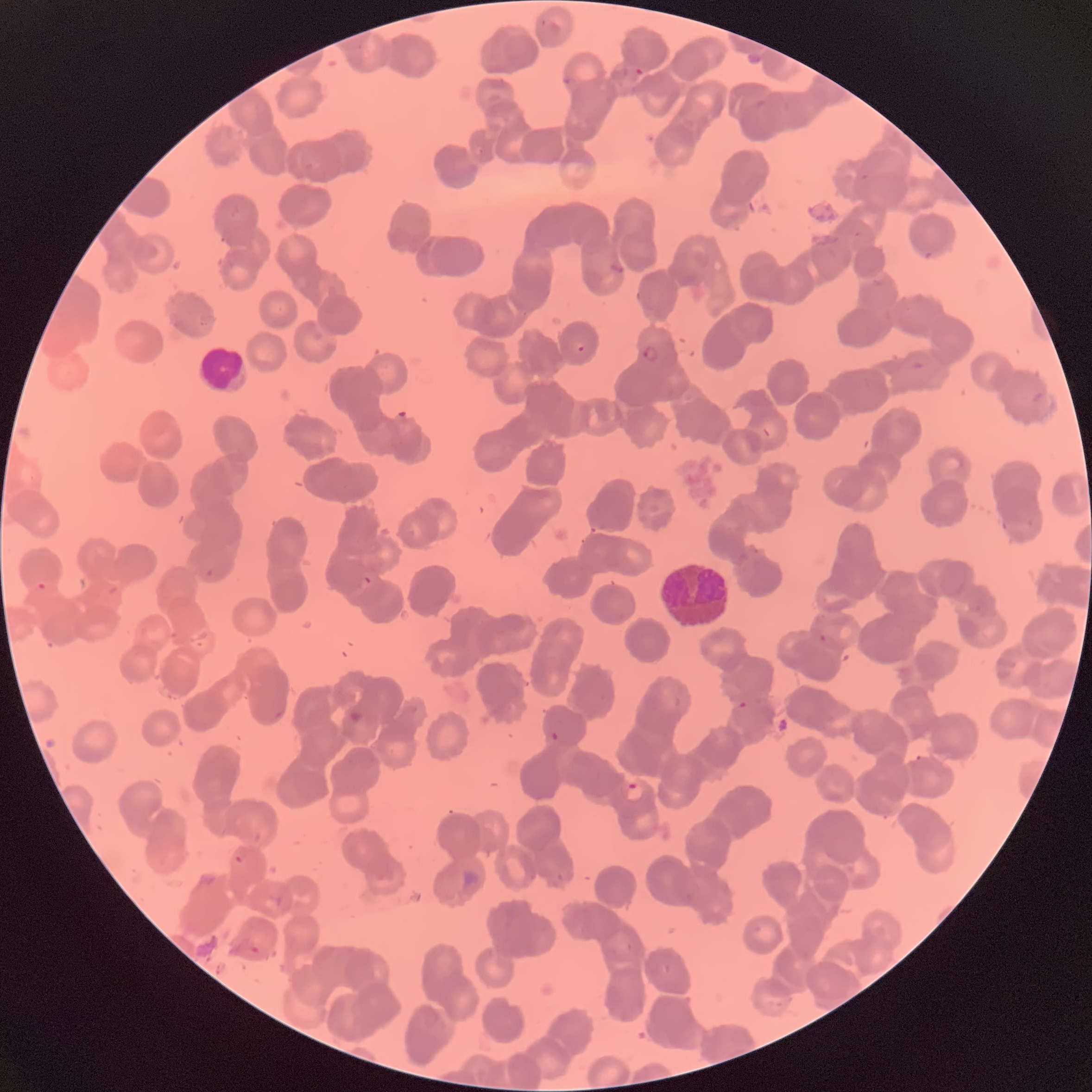

Summary:
  - Coordinate format: approximate bounding boxes as named x1/y1/x2/y2 corners in pixels
  - White blood cell locations: (x1=199, y1=344, x2=248, y2=395)
  - Plasmodium parasite locations: (x1=634, y1=67, x2=645, y2=77), (x1=560, y1=74, x2=573, y2=87), (x1=610, y1=256, x2=624, y2=274), (x1=577, y1=342, x2=586, y2=353), (x1=643, y1=344, x2=660, y2=364), (x1=205, y1=568, x2=215, y2=577), (x1=362, y1=576, x2=373, y2=585), (x1=36, y1=581, x2=47, y2=591), (x1=817, y1=634, x2=842, y2=652), (x1=737, y1=700, x2=747, y2=710), (x1=550, y1=731, x2=560, y2=742), (x1=625, y1=779, x2=643, y2=801), (x1=234, y1=855, x2=244, y2=865)
  - Modality: optical microscopy
  - Preparation: thin blood smear
  - Image size: 1092×1092 pixels
  - Red blood cell morphology: rouleaux formation